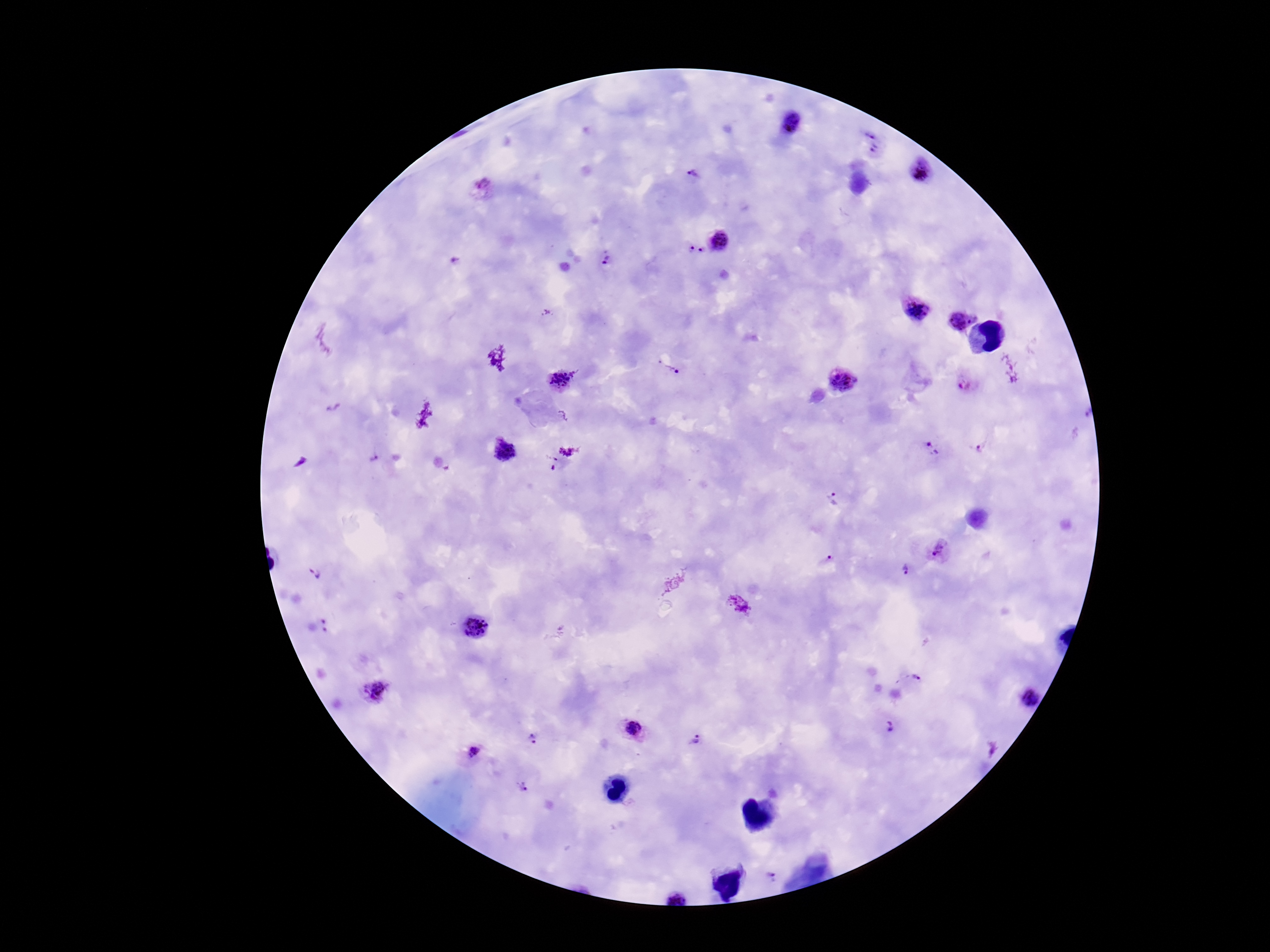
Approximate centers as (x, y) in pixels.
Summary:
  - Plasmodium parasite locations: (791, 122), (871, 144), (924, 173), (692, 174), (720, 239), (689, 248), (703, 250), (607, 260), (916, 312), (963, 317), (672, 366), (559, 380), (845, 380), (968, 384), (981, 445), (930, 448), (504, 449), (834, 501), (939, 550), (830, 560), (905, 570), (315, 574), (738, 604), (475, 627), (915, 677), (375, 692), (1029, 698), (634, 728), (889, 728), (534, 738), (696, 740), (474, 751), (523, 787), (773, 875), (677, 896)
  - Preparation: thick peripheral-blood smear
  - Patient malaria status: positive
  - Image size: 1270×952 pixels
  - Field of view: one from this slide
  - Magnification: 100x
  - Stain: Giemsa
  - Capture: smartphone camera through the microscope eyepiece